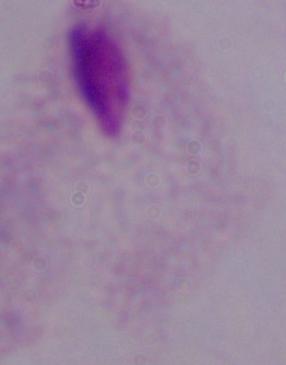

{
  "identification": "trichomonad",
  "modality": "photomicrograph",
  "magnification": "1000x"
}